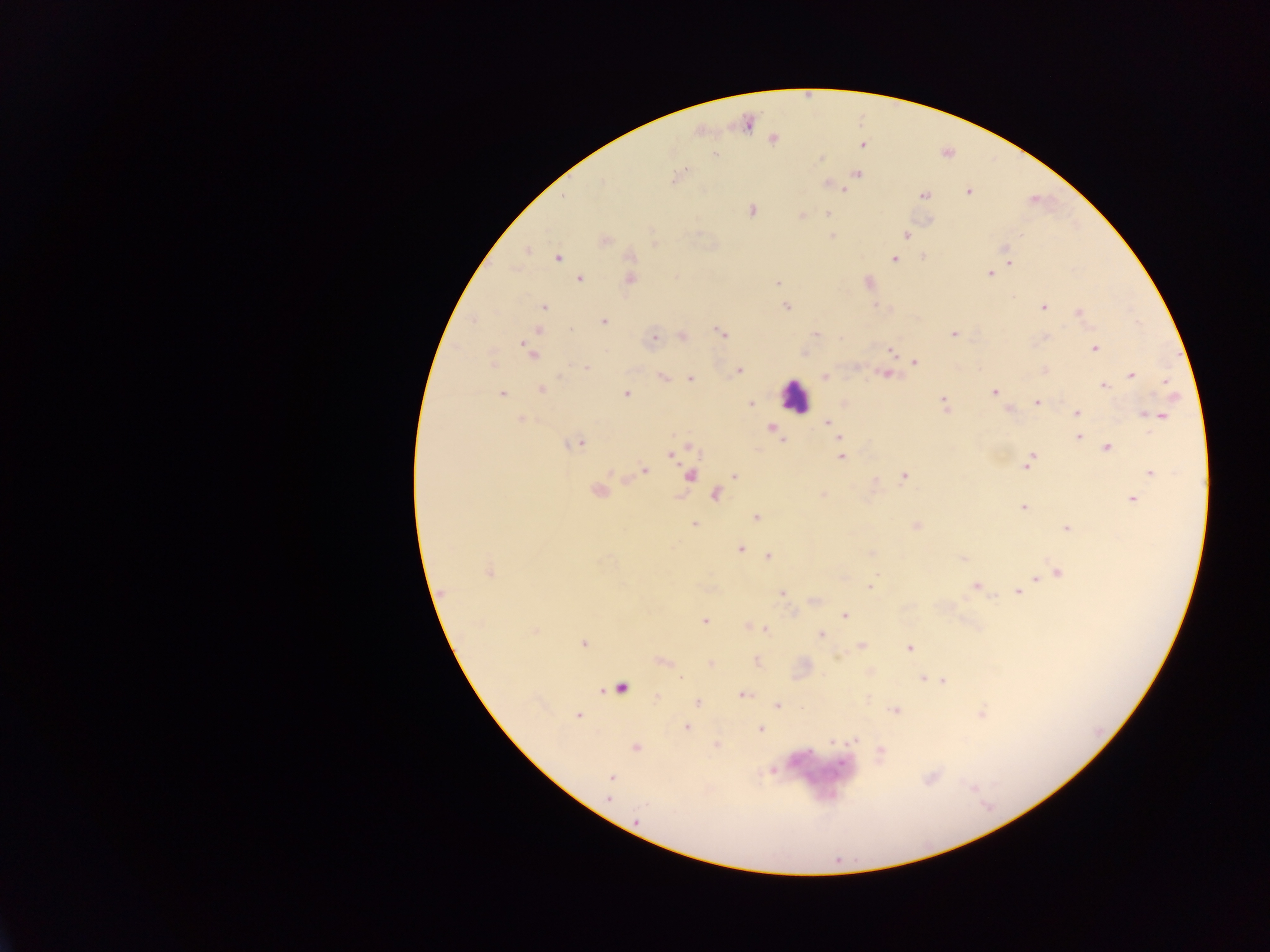

Approximate centers as (x, y) in pixels. Leukocyte locations: (794, 396), (623, 684). Malaria parasite locations: (773, 139), (862, 144), (716, 155), (819, 159), (857, 173), (677, 176), (829, 184), (969, 192), (924, 195), (752, 210), (827, 214), (802, 215), (906, 235), (1021, 235), (832, 236), (604, 240), (1004, 249), (526, 251), (559, 257), (631, 257), (924, 257), (894, 259), (1011, 262), (989, 273), (580, 279), (630, 279), (867, 282), (777, 283), (543, 307), (786, 307), (1043, 307), (1078, 312), (604, 321), (538, 331), (721, 333), (815, 333), (953, 334), (683, 337), (653, 339), (1094, 348), (890, 351), (530, 352), (915, 362), (493, 365), (587, 368), (1044, 370), (739, 371), (885, 374), (1132, 374), (825, 376), (662, 377), (690, 379), (1166, 382), (1104, 386), (542, 389), (993, 391), (502, 394), (626, 394), (944, 400), (1037, 402), (751, 403), (1010, 410), (1077, 413), (1158, 415), (520, 419), (828, 421), (832, 427), (773, 428), (1079, 436), (839, 438), (577, 443), (1108, 448), (671, 454), (1032, 455), (841, 457), (1028, 464), (644, 470), (1150, 473), (734, 476), (689, 477), (903, 478), (598, 492), (716, 495), (823, 495), (1132, 499), (1023, 507), (756, 517), (694, 525), (916, 525), (1066, 528), (740, 548), (870, 553), (768, 556), (963, 558), (488, 572), (1059, 573), (1036, 578), (976, 586), (869, 587), (1018, 592), (444, 593), (781, 593), (845, 615), (704, 621), (764, 629), (535, 631), (821, 635), (583, 643), (862, 645), (909, 648), (662, 661), (757, 662), (711, 664), (680, 678), (923, 679), (934, 679), (942, 680), (743, 695), (657, 697), (697, 702), (777, 706), (895, 711), (578, 715), (686, 728), (760, 729), (856, 739), (832, 741), (635, 748), (880, 752), (842, 763), (773, 770), (611, 778), (608, 799), (637, 819). Image is 1270×952 pixels. Thick blood smear. Single field of view. Collected in Ghana. Mobile-phone photograph taken through the microscope.